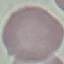

Summary:
  - Result: negative for malaria parasites
  - Image type: cell patch, automatically extracted from a larger field of view and resized to 64 × 64 pixels
  - Stain: Giemsa
  - Preparation: thin smear
  - Capture: smartphone camera at the microscope eyepiece